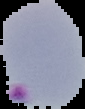 The area outside the segmented cell region is set to black. Result: Plasmodium parasites identified. From a thin blood film. Image is 85×109 pixels.